Name the cell type shown.
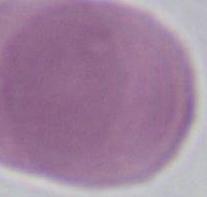

This is an erythrocyte.

Captured at 1000x magnification. Micrograph.